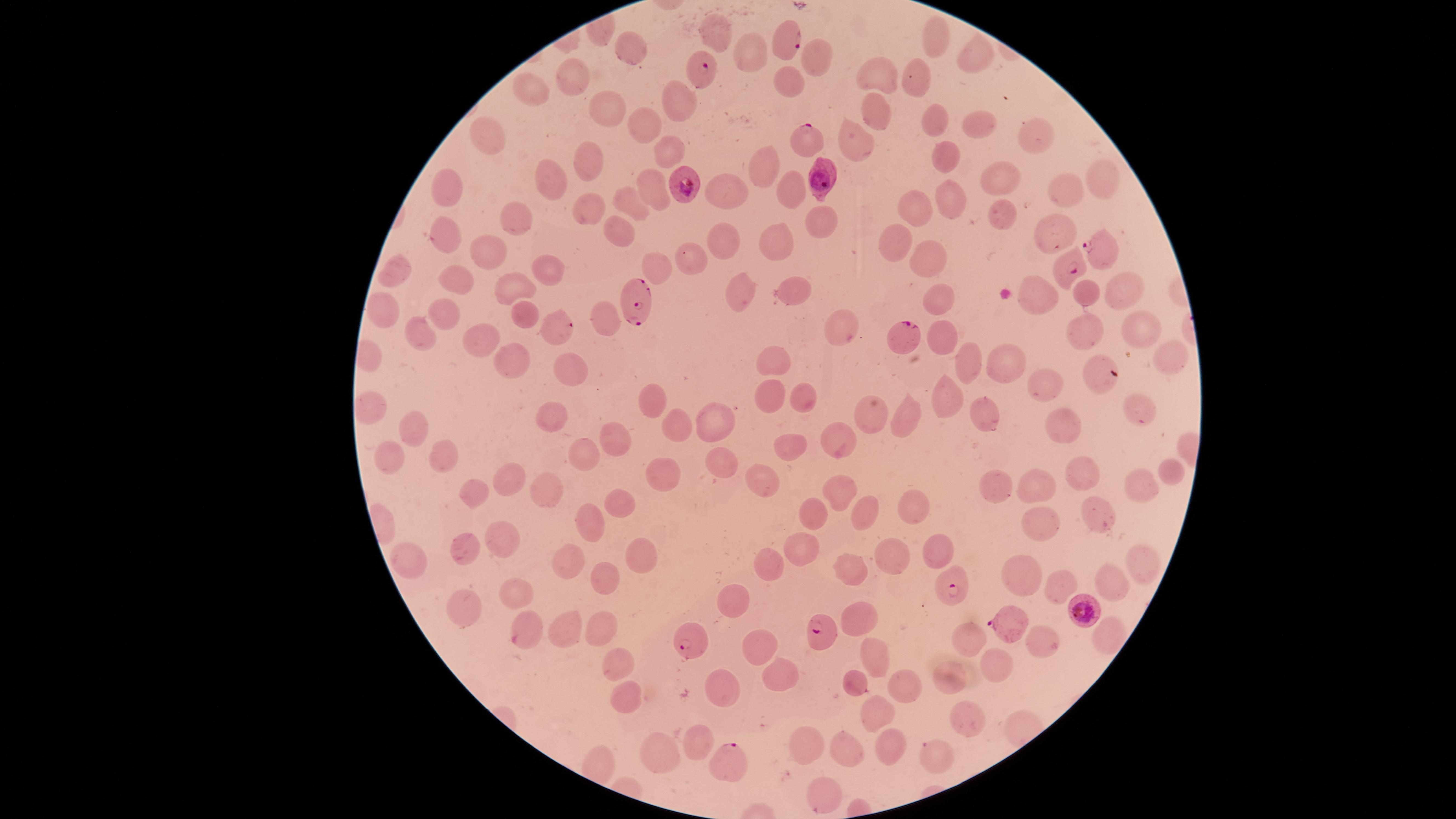
Approximate marker points, in pixels from the top-left corner. Parasitized red blood cells: (x=784, y=42), (x=701, y=68), (x=802, y=137), (x=822, y=177), (x=683, y=185), (x=1095, y=250), (x=1068, y=271), (x=635, y=303), (x=560, y=325), (x=907, y=335), (x=952, y=583), (x=1082, y=609), (x=1009, y=625), (x=826, y=631), (x=692, y=638), (x=727, y=759). Uninfected red blood cells: (x=715, y=30), (x=933, y=36), (x=635, y=51), (x=812, y=58), (x=973, y=58), (x=747, y=59), (x=874, y=72), (x=920, y=78), (x=575, y=83), (x=788, y=84), (x=530, y=94), (x=675, y=105), (x=607, y=109), (x=877, y=111), (x=935, y=117), (x=645, y=124), (x=973, y=124), (x=1040, y=125), (x=490, y=139), (x=856, y=145), (x=668, y=148), (x=587, y=157), (x=946, y=159), (x=763, y=174), (x=1100, y=177), (x=1000, y=179), (x=549, y=184), (x=721, y=190), (x=1065, y=190), (x=448, y=192), (x=789, y=192), (x=650, y=195), (x=950, y=198), (x=631, y=204), (x=585, y=212), (x=915, y=212), (x=1004, y=217), (x=519, y=220), (x=819, y=220), (x=616, y=230), (x=447, y=234), (x=1056, y=234), (x=722, y=239), (x=779, y=241), (x=897, y=249), (x=483, y=250), (x=689, y=256), (x=930, y=258), (x=656, y=266), (x=542, y=268), (x=392, y=270), (x=456, y=276), (x=1114, y=280), (x=519, y=287), (x=1086, y=292), (x=795, y=293), (x=735, y=295), (x=939, y=300), (x=382, y=306), (x=443, y=311), (x=517, y=315), (x=603, y=322), (x=843, y=324), (x=1139, y=325), (x=420, y=331), (x=1086, y=333), (x=938, y=339), (x=470, y=340), (x=509, y=355), (x=1164, y=355), (x=774, y=360), (x=964, y=360), (x=999, y=363), (x=569, y=369), (x=1100, y=377), (x=1047, y=388), (x=947, y=391), (x=804, y=394), (x=652, y=398), (x=767, y=398), (x=369, y=410), (x=718, y=410), (x=1142, y=410), (x=988, y=411), (x=905, y=413), (x=864, y=414), (x=551, y=415), (x=414, y=425), (x=1058, y=426), (x=677, y=427), (x=614, y=436), (x=835, y=446), (x=586, y=448), (x=789, y=454), (x=723, y=457), (x=442, y=459), (x=388, y=461), (x=1092, y=471), (x=1169, y=472), (x=661, y=473), (x=757, y=479), (x=513, y=481), (x=1002, y=482), (x=1038, y=482), (x=1143, y=482), (x=548, y=487), (x=477, y=489), (x=836, y=492), (x=616, y=499), (x=911, y=509), (x=1089, y=513), (x=860, y=514), (x=821, y=517), (x=1041, y=519), (x=587, y=520), (x=502, y=531), (x=802, y=547), (x=637, y=548), (x=934, y=548), (x=458, y=550), (x=407, y=555), (x=894, y=557), (x=568, y=558), (x=1136, y=561), (x=766, y=562), (x=850, y=568), (x=1020, y=570), (x=604, y=572), (x=1110, y=578), (x=1058, y=584), (x=528, y=591), (x=734, y=599), (x=463, y=606), (x=860, y=614), (x=594, y=623), (x=564, y=625), (x=525, y=627), (x=1104, y=636), (x=971, y=637), (x=756, y=640), (x=1046, y=641), (x=871, y=652), (x=618, y=661), (x=999, y=663), (x=784, y=674), (x=945, y=674), (x=852, y=679), (x=904, y=684), (x=721, y=685), (x=624, y=699), (x=876, y=712), (x=966, y=716), (x=699, y=736), (x=805, y=738), (x=889, y=741), (x=850, y=746), (x=663, y=748), (x=938, y=758), (x=828, y=791). Presence: malaria parasites identified. Giemsa stain. The visible region is circular. One field of view of the specimen. Smartphone photograph through the microscope eyepiece. Image is 1456×819 pixels. Thin blood smear. Species: Plasmodium falciparum.